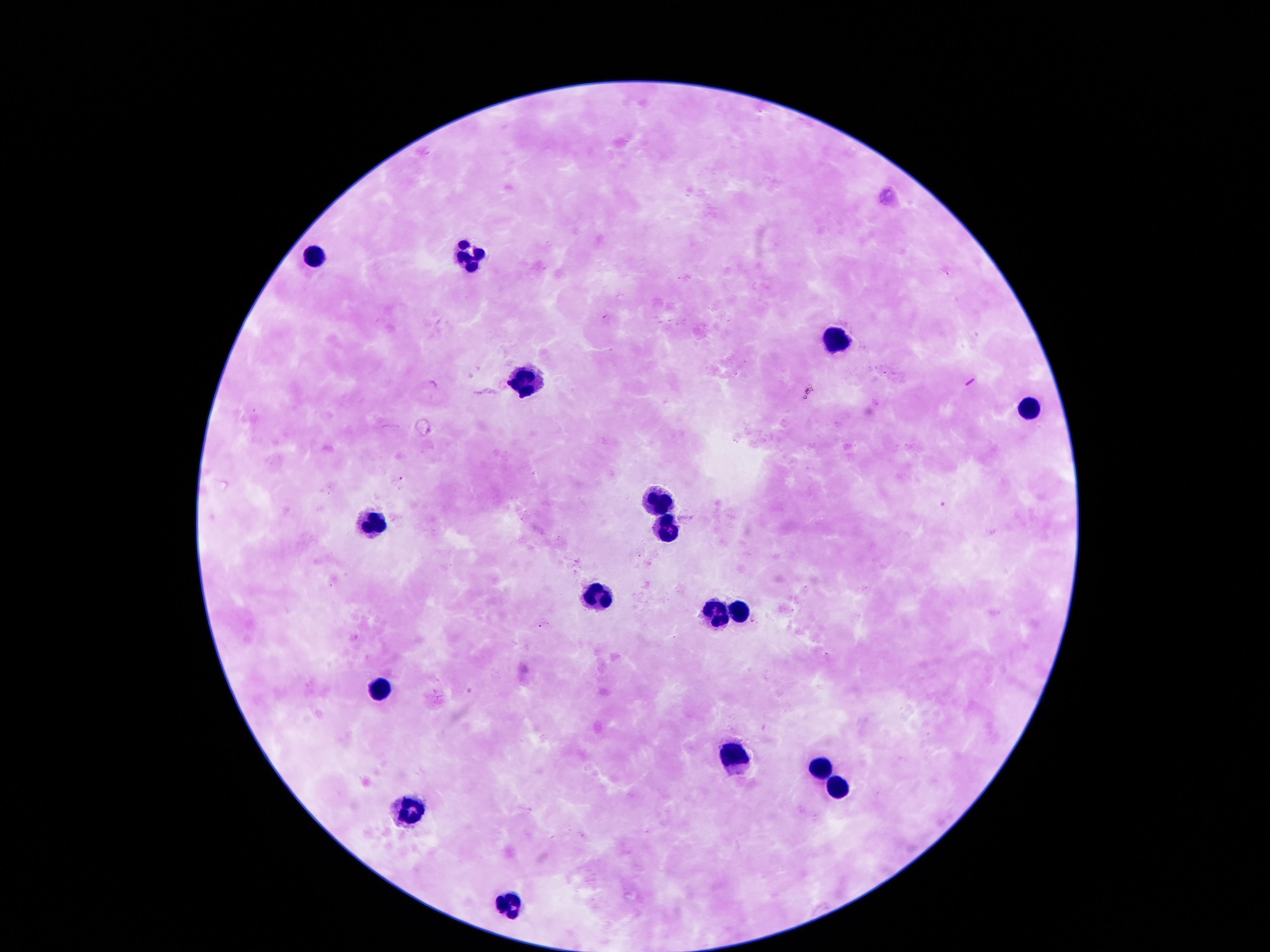

capture: smartphone camera through the microscope eyepiece
magnification: 100x
stain: Giemsa
field_of_view: one from this slide
preparation: thick blood smear
patient_malaria_status: not infected
leukocyte_locations: 'approximate centers as {x, y} in pixels: {471, 251}, {313, 256}, {837, 340}, {518, 382}, {1025, 409}, {662, 503}, {363, 526}, {662, 526}, {592, 592}, {713, 610}, {736, 610}, {380, 684}, {733, 762}, {824, 765}, {837, 788}, {413, 815}, {514, 899}'
image_size: 1270×952 pixels